Report the malaria status of this cell.
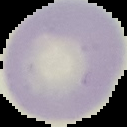

It is uninfected.

Summary:
  - Preparation: thin blood film
  - Image type: segmented cell region on a black background
  - Image size: 127×127 pixels